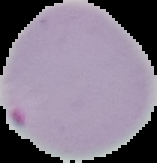

Summary:
  - Malaria status: parasitized
  - Preparation: thin blood film
  - Image size: 157×163 pixels
  - Image type: cell region segmented out of the field of view; surrounding area masked to black